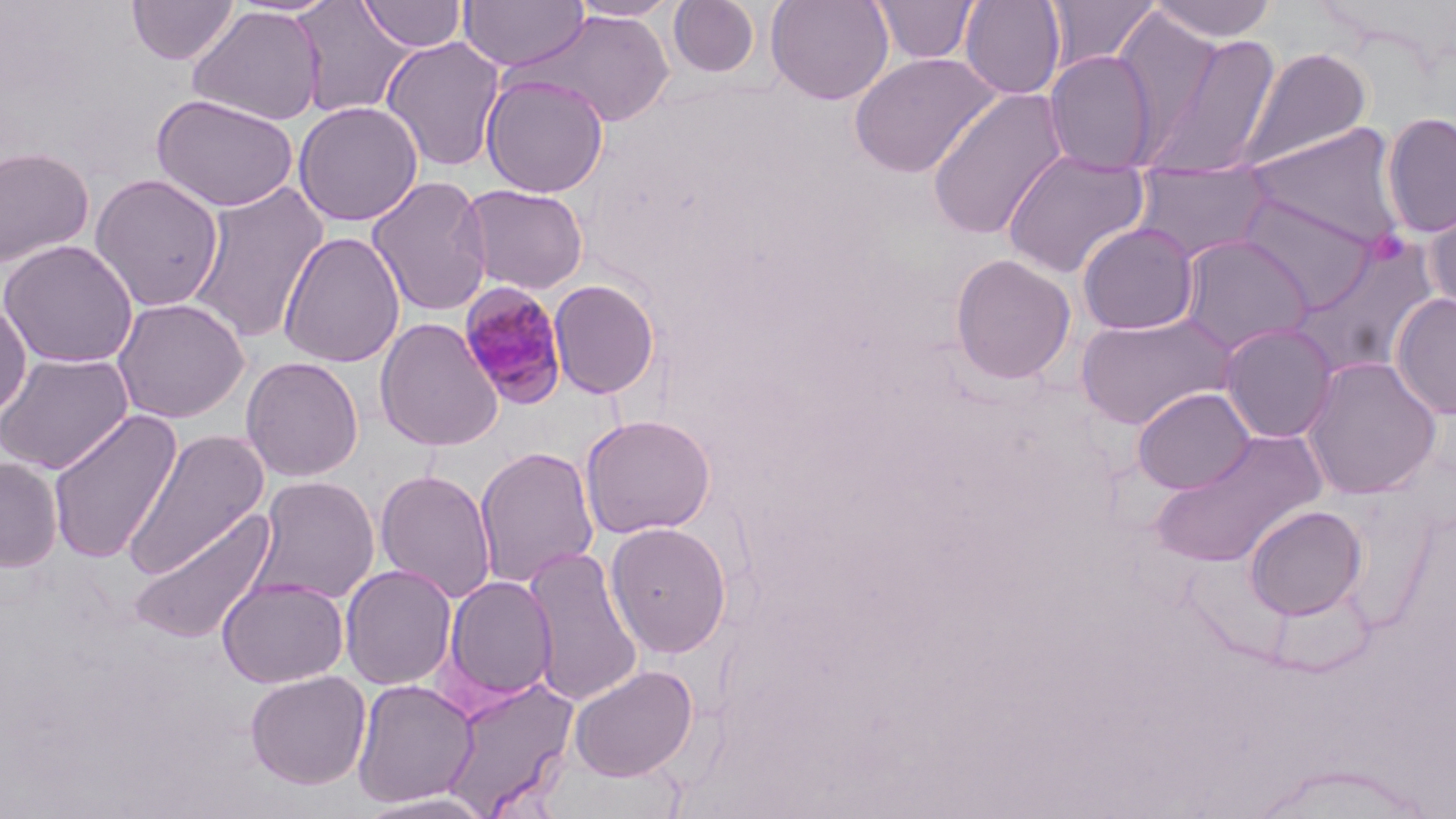
Approximate bounding boxes as (x1, y1, x2, y2) in pixels. Uninfected red blood cell locations: (126, 0, 239, 65), (568, 0, 681, 21), (668, 0, 761, 80), (765, 0, 894, 105), (870, 0, 979, 65), (959, 0, 1067, 100), (1045, 0, 1161, 72), (1148, 0, 1279, 43), (291, 1, 416, 118), (357, 1, 468, 53), (459, 1, 590, 72), (187, 5, 325, 126), (517, 9, 676, 128), (1112, 10, 1224, 152), (1137, 30, 1284, 179), (380, 36, 505, 172), (1236, 47, 1372, 173), (1045, 50, 1157, 175), (848, 51, 1001, 178), (480, 73, 609, 198), (926, 87, 1070, 241), (151, 94, 299, 212), (293, 100, 423, 226), (1381, 111, 1456, 239), (1247, 123, 1407, 249), (0, 146, 95, 269), (1002, 149, 1151, 279), (1131, 161, 1274, 262), (89, 173, 225, 311), (366, 176, 492, 317), (186, 180, 329, 344), (460, 184, 589, 295), (1237, 192, 1380, 313), (1423, 192, 1456, 319), (1077, 222, 1200, 336), (278, 231, 405, 368), (1177, 234, 1315, 357), (1292, 235, 1442, 378), (0, 240, 139, 369), (949, 253, 1076, 385), (548, 278, 661, 399), (1390, 292, 1456, 420), (0, 295, 32, 420), (112, 297, 250, 423), (1074, 310, 1238, 429), (374, 318, 504, 452), (1218, 322, 1339, 443), (0, 351, 134, 475), (1301, 355, 1442, 499), (241, 356, 364, 482), (1131, 387, 1256, 495), (47, 408, 183, 565), (580, 414, 716, 538), (122, 428, 271, 580), (1150, 429, 1328, 567), (475, 446, 599, 589), (0, 457, 63, 572), (374, 469, 497, 604), (252, 476, 380, 605), (1243, 504, 1368, 620), (128, 506, 277, 646), (604, 521, 733, 658), (523, 544, 644, 708), (340, 563, 457, 690), (217, 575, 350, 689), (442, 576, 558, 704), (568, 664, 698, 781), (245, 670, 371, 790), (435, 676, 578, 817), (351, 678, 478, 808), (552, 762, 690, 818), (356, 790, 499, 818). Plasmodium malariae-infected red blood cell locations: (459, 282, 569, 409). Slide-level diagnosis: Plasmodium malariae. Thin blood film. Optical microscopy. 1000x magnification. Image is 1456×819 pixels. One field of a larger specimen. May-Grünwald-Giemsa stain.